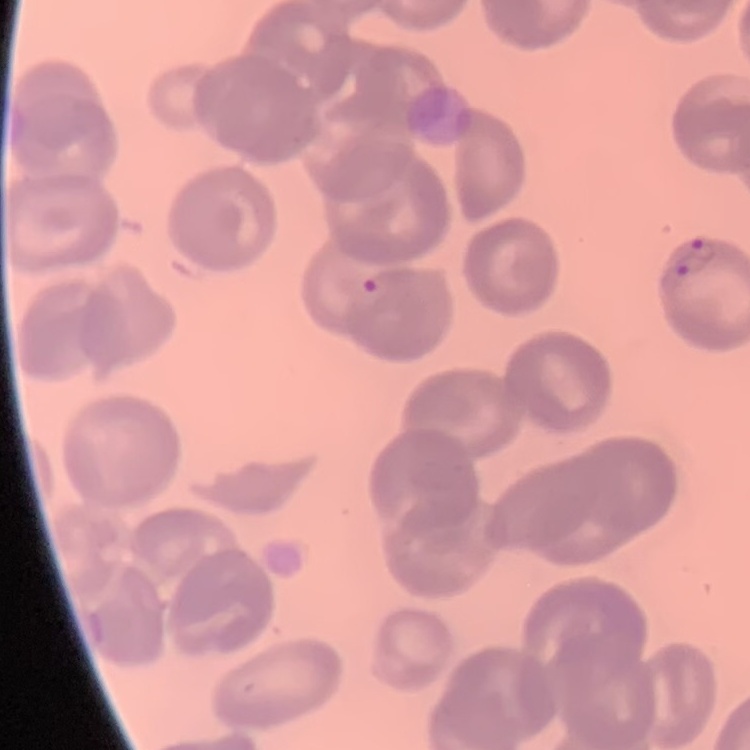

erythrocyte morphology = no rouleaux formation
stain = Field's or Giemsa
image type = square crop of a larger photomicrograph
preparation = thin peripheral smear